Locate every Plasmodium vivax-infected red blood cell.
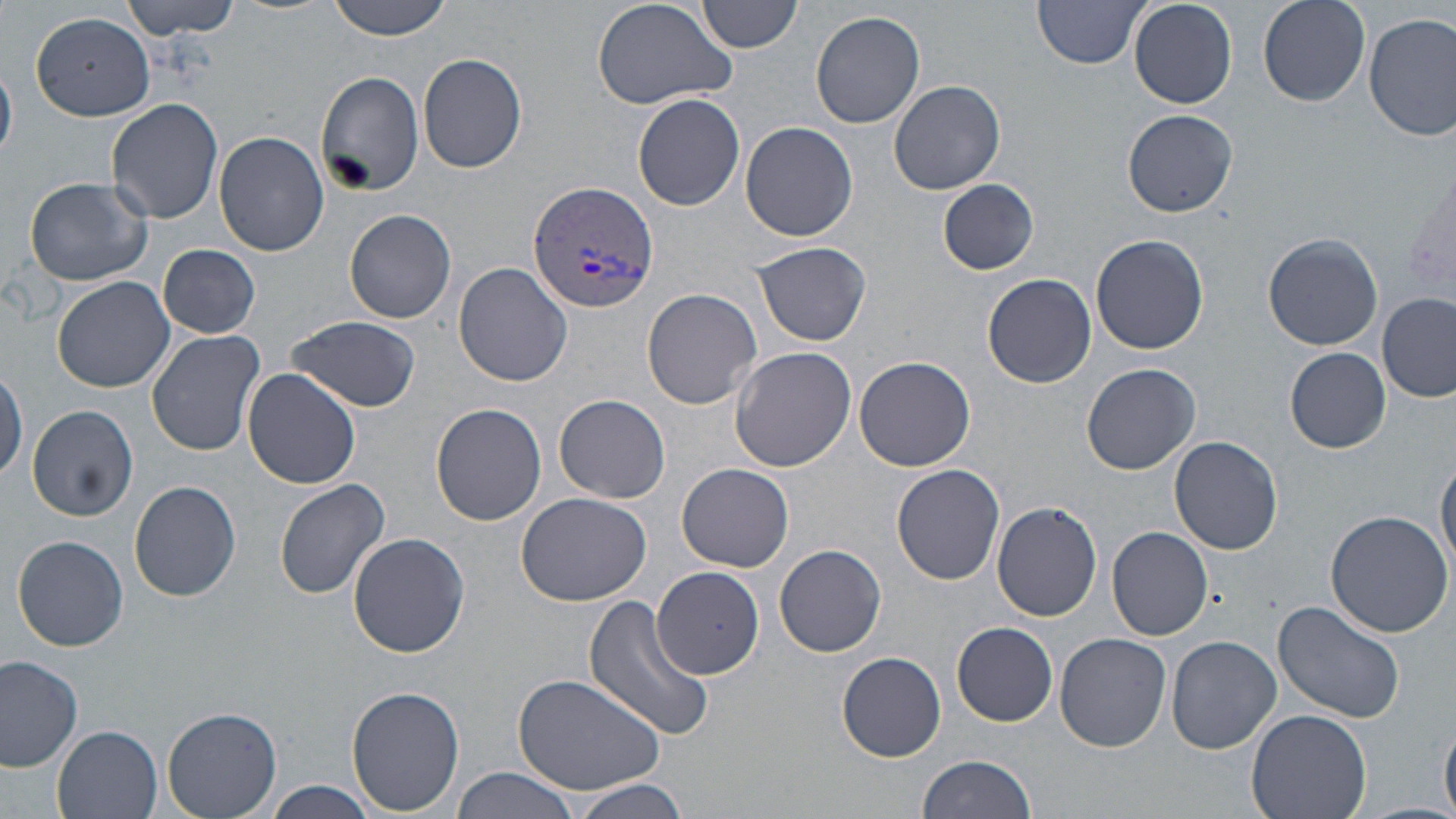

Approximate bounding boxes as (x1, y1, x2, y2) in pixels.
Plasmodium vivax-infected red blood cells: (529, 182, 662, 315).

Uninfected red blood cell locations: (117, 0, 242, 39), (328, 0, 453, 40), (590, 0, 738, 113), (697, 0, 801, 54), (1034, 0, 1153, 68), (1130, 0, 1236, 108), (1258, 0, 1370, 107), (811, 10, 925, 129), (30, 12, 156, 121), (1365, 14, 1456, 143), (417, 51, 527, 173), (1, 58, 18, 164), (315, 71, 426, 195), (889, 80, 1005, 194), (633, 93, 745, 211), (109, 99, 224, 224), (1122, 108, 1238, 217), (739, 121, 860, 242), (214, 131, 328, 256), (24, 175, 153, 287), (937, 179, 1039, 274), (345, 209, 458, 323), (1263, 232, 1385, 349), (1092, 235, 1210, 356), (751, 240, 873, 346), (157, 243, 261, 339), (454, 261, 574, 387), (984, 274, 1097, 388), (52, 276, 176, 393), (641, 288, 763, 410), (1379, 293, 1455, 403), (287, 316, 421, 413), (146, 329, 265, 456), (729, 346, 855, 471), (1286, 348, 1390, 453), (853, 355, 976, 471), (1082, 363, 1201, 476), (0, 365, 27, 484), (243, 369, 361, 491), (554, 393, 671, 503), (430, 404, 547, 526), (28, 405, 137, 521), (1170, 435, 1284, 555), (1436, 453, 1456, 571), (676, 463, 795, 571), (892, 463, 1006, 585), (274, 478, 391, 599), (129, 481, 242, 603), (515, 490, 654, 606), (991, 501, 1103, 622), (1325, 511, 1454, 639), (1106, 526, 1213, 640), (346, 532, 470, 658), (12, 534, 130, 652), (774, 543, 887, 658), (652, 566, 763, 677), (583, 595, 715, 742), (1271, 599, 1406, 722), (953, 621, 1058, 726), (1178, 622, 1376, 747), (1057, 633, 1171, 753), (1167, 636, 1283, 754), (838, 651, 947, 762), (0, 656, 83, 771), (511, 669, 669, 796), (346, 684, 466, 814), (160, 706, 284, 819), (1247, 708, 1371, 819), (1441, 710, 1456, 817), (55, 726, 160, 819), (916, 754, 1038, 819), (451, 767, 586, 819), (569, 777, 693, 819), (261, 782, 379, 817). Slide-level diagnosis: Plasmodium vivax. Optical microscopy. May-Grünwald-Giemsa-stained preparation. One field of a larger specimen. Thin blood film. Image is 1456×819 pixels. 1000x magnification.